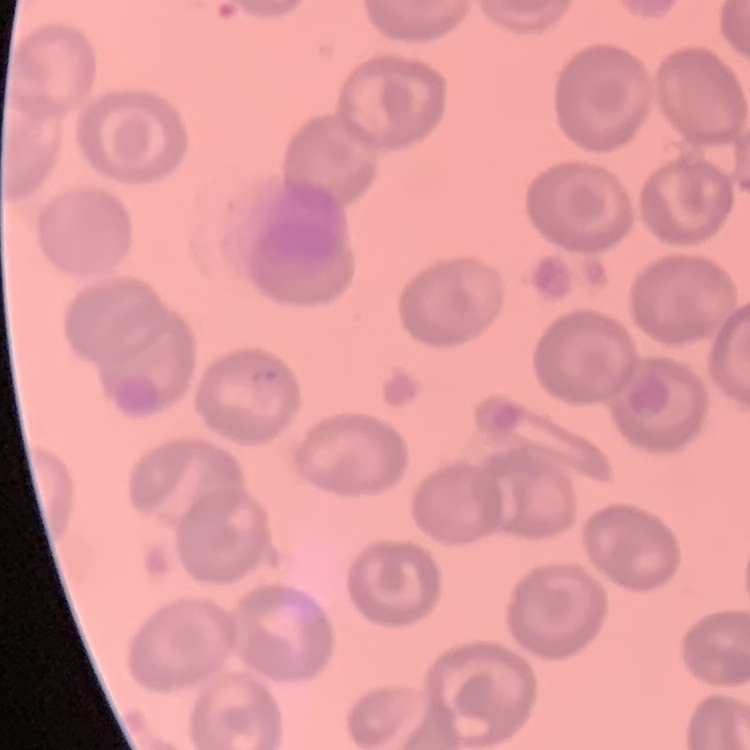

{
  "erythrocyte_morphology": "no rouleaux formation",
  "preparation": "thin blood smear",
  "image_type": "one tile cut from a larger photomicrograph",
  "stain": "Field's or Giemsa"
}